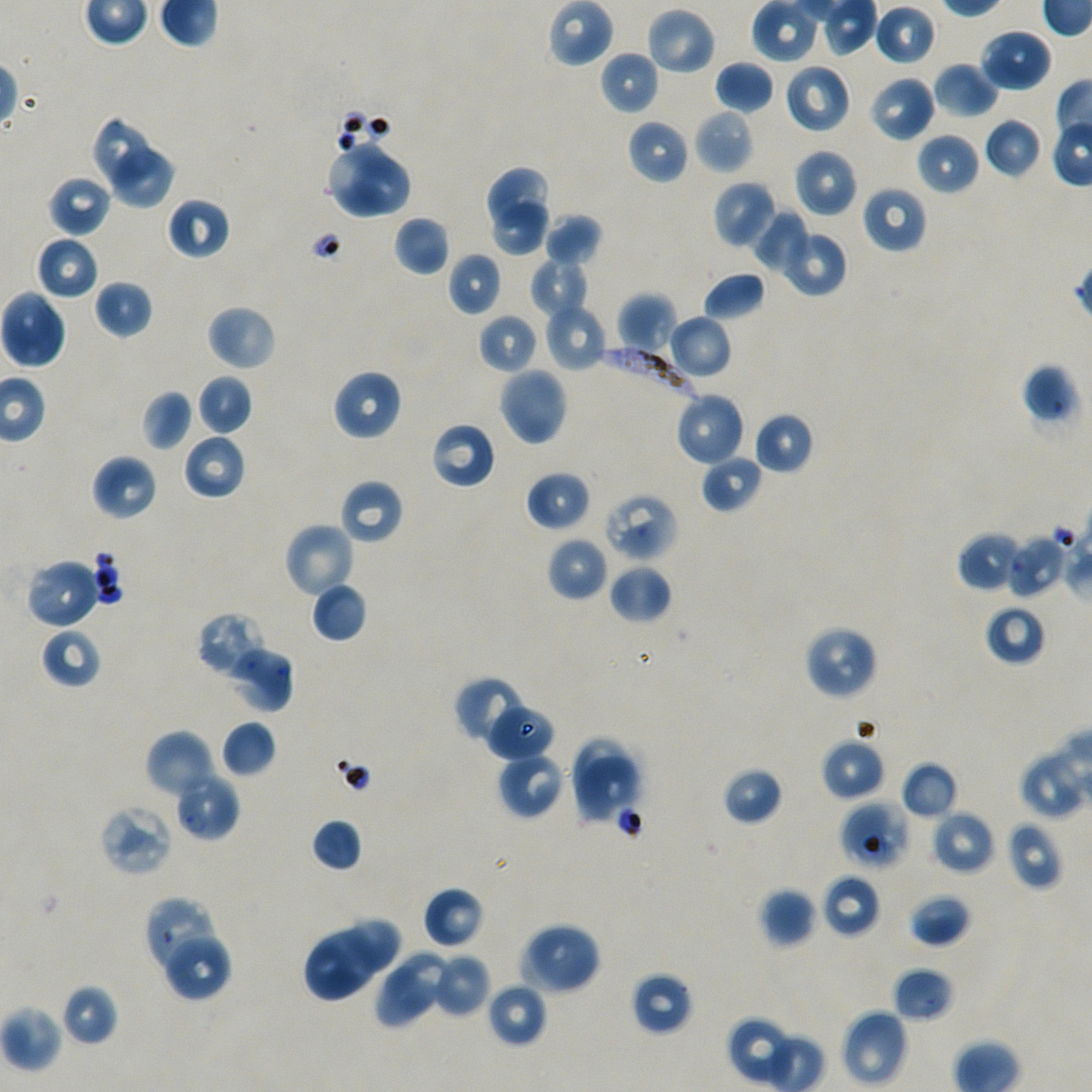
Approximate bounding rectangles given as corner coordinates in pixels from the top-left. Not every red blood cell is marked. A life-cycle stage — or a range of stages, where the recorded stages span more than one — follows each staged infected red blood cell.
Summary:
  - Locations of uninfected red blood cells: (x1=752, y1=0, x2=820, y2=63), (x1=874, y1=3, x2=936, y2=67), (x1=645, y1=6, x2=716, y2=76), (x1=979, y1=28, x2=1053, y2=92), (x1=599, y1=50, x2=660, y2=115), (x1=714, y1=60, x2=775, y2=114), (x1=932, y1=61, x2=1000, y2=118), (x1=784, y1=63, x2=852, y2=134), (x1=869, y1=75, x2=936, y2=143), (x1=693, y1=108, x2=754, y2=175), (x1=91, y1=114, x2=157, y2=187), (x1=983, y1=117, x2=1042, y2=178), (x1=626, y1=119, x2=689, y2=185), (x1=916, y1=132, x2=981, y2=196), (x1=325, y1=140, x2=390, y2=219), (x1=106, y1=147, x2=179, y2=213), (x1=793, y1=148, x2=858, y2=218), (x1=352, y1=154, x2=413, y2=219), (x1=487, y1=165, x2=551, y2=227), (x1=47, y1=175, x2=113, y2=237), (x1=712, y1=180, x2=778, y2=250), (x1=862, y1=185, x2=928, y2=254), (x1=166, y1=197, x2=230, y2=261), (x1=490, y1=201, x2=553, y2=257), (x1=750, y1=205, x2=809, y2=274), (x1=543, y1=213, x2=604, y2=268), (x1=393, y1=215, x2=450, y2=276), (x1=779, y1=228, x2=848, y2=297), (x1=35, y1=236, x2=99, y2=300), (x1=446, y1=252, x2=503, y2=316), (x1=530, y1=257, x2=588, y2=318), (x1=702, y1=270, x2=766, y2=322), (x1=93, y1=279, x2=153, y2=338), (x1=0, y1=290, x2=67, y2=369), (x1=617, y1=292, x2=677, y2=355), (x1=545, y1=302, x2=611, y2=371), (x1=206, y1=304, x2=277, y2=371), (x1=477, y1=314, x2=538, y2=374), (x1=667, y1=314, x2=732, y2=378), (x1=1021, y1=363, x2=1080, y2=428), (x1=498, y1=366, x2=568, y2=447), (x1=332, y1=369, x2=403, y2=441), (x1=196, y1=374, x2=253, y2=435), (x1=141, y1=389, x2=194, y2=452), (x1=674, y1=391, x2=746, y2=467), (x1=753, y1=411, x2=814, y2=475), (x1=430, y1=421, x2=496, y2=490), (x1=183, y1=433, x2=246, y2=500), (x1=700, y1=453, x2=763, y2=513), (x1=90, y1=454, x2=158, y2=521), (x1=525, y1=471, x2=591, y2=532), (x1=339, y1=479, x2=404, y2=545), (x1=283, y1=522, x2=357, y2=600), (x1=958, y1=531, x2=1024, y2=593), (x1=547, y1=536, x2=609, y2=602), (x1=24, y1=558, x2=103, y2=630), (x1=608, y1=563, x2=672, y2=623), (x1=310, y1=581, x2=368, y2=643), (x1=984, y1=603, x2=1046, y2=666), (x1=196, y1=611, x2=272, y2=681), (x1=803, y1=625, x2=878, y2=700), (x1=41, y1=627, x2=102, y2=690), (x1=454, y1=675, x2=530, y2=746), (x1=487, y1=704, x2=554, y2=761), (x1=221, y1=720, x2=277, y2=778), (x1=144, y1=729, x2=216, y2=799), (x1=570, y1=737, x2=633, y2=799), (x1=820, y1=738, x2=886, y2=801), (x1=497, y1=752, x2=566, y2=820), (x1=575, y1=755, x2=641, y2=821), (x1=1018, y1=755, x2=1081, y2=819), (x1=900, y1=761, x2=958, y2=820), (x1=722, y1=767, x2=784, y2=826), (x1=929, y1=809, x2=996, y2=876), (x1=311, y1=818, x2=363, y2=871), (x1=1005, y1=821, x2=1064, y2=892), (x1=822, y1=873, x2=881, y2=937), (x1=423, y1=886, x2=485, y2=948), (x1=759, y1=888, x2=816, y2=947), (x1=908, y1=893, x2=970, y2=948), (x1=346, y1=915, x2=401, y2=974), (x1=517, y1=922, x2=602, y2=996), (x1=161, y1=929, x2=232, y2=1001), (x1=303, y1=930, x2=376, y2=1002), (x1=394, y1=951, x2=454, y2=1013), (x1=431, y1=953, x2=490, y2=1017), (x1=892, y1=966, x2=954, y2=1023), (x1=375, y1=968, x2=440, y2=1029), (x1=631, y1=972, x2=694, y2=1036), (x1=485, y1=982, x2=547, y2=1048), (x1=60, y1=983, x2=118, y2=1046), (x1=0, y1=1004, x2=64, y2=1073), (x1=840, y1=1008, x2=909, y2=1088), (x1=727, y1=1016, x2=796, y2=1085)
  - Locations of red blood cells of indeterminate infection status: (x1=602, y1=492, x2=679, y2=562), (x1=1007, y1=534, x2=1067, y2=598), (x1=222, y1=643, x2=294, y2=713), (x1=840, y1=801, x2=910, y2=870), (x1=98, y1=804, x2=174, y2=877), (x1=143, y1=896, x2=221, y2=977)
  - Locations of infected red blood cells: (x1=597, y1=344, x2=708, y2=408); (x1=174, y1=770, x2=240, y2=841) ring
  - Objective: 100x, oil immersion, numerical aperture 1.45
  - Preparation: thin blood smear
  - Culture: static in-vitro Plasmodium falciparum strain NF54
  - Stain: Giemsa
  - Image size: 1092×1092 pixels
  - Donor blood group: A+/O+
  - Field of view: one from this slide